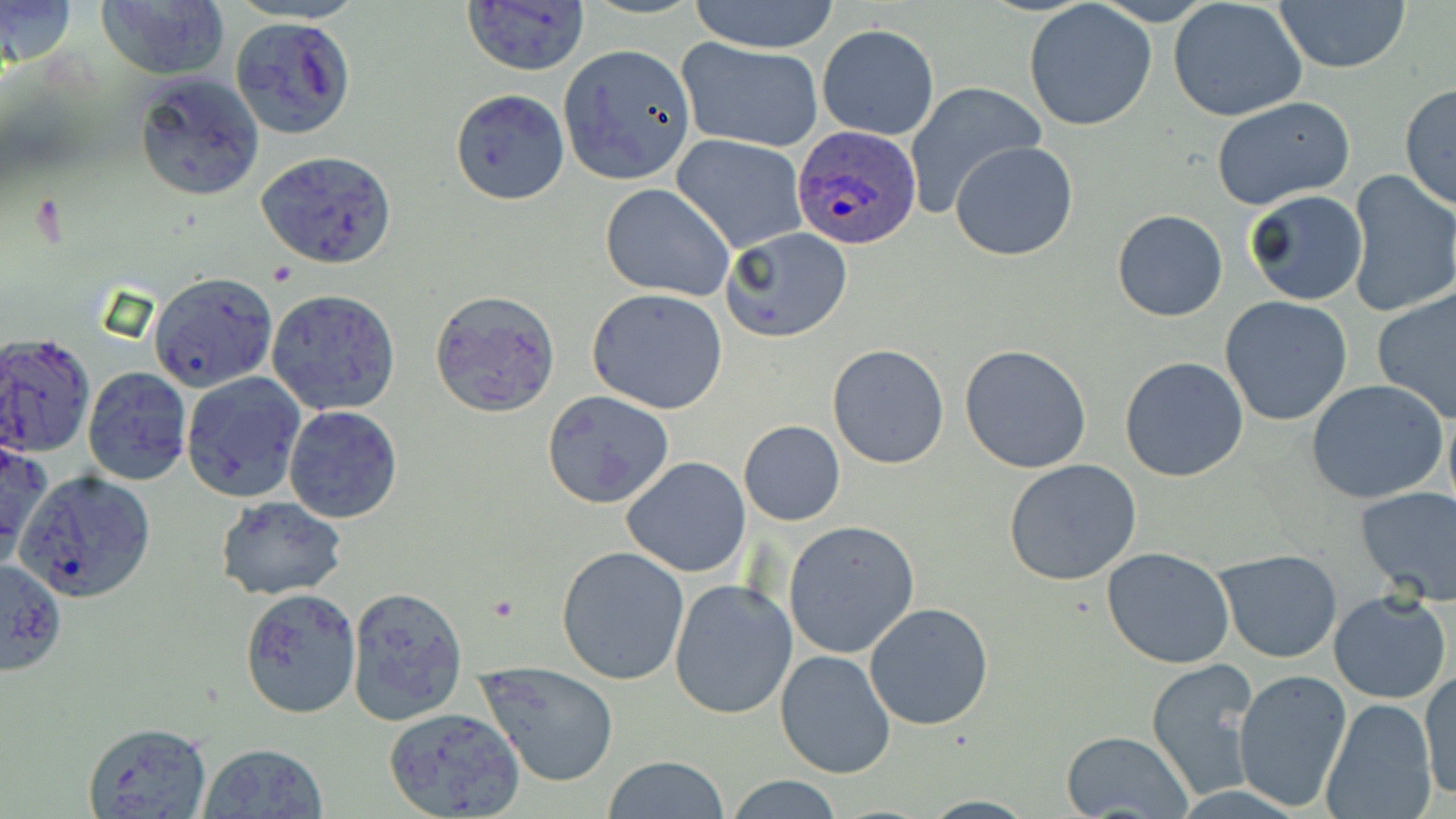 Approximate bounding boxes as (x1, y1, x2, y2) in pixels. Plasmodium ovale-infected red blood cell locations: (792, 123, 926, 251). Uninfected red blood cell locations: (0, 0, 78, 69), (464, 0, 588, 74), (688, 0, 838, 53), (1272, 0, 1412, 72), (1169, 1, 1307, 122), (96, 2, 229, 81), (1022, 2, 1158, 132), (230, 18, 357, 140), (818, 23, 940, 140), (678, 38, 825, 154), (559, 44, 697, 183), (137, 74, 263, 201), (903, 81, 1043, 218), (1399, 82, 1456, 211), (449, 88, 569, 206), (1210, 94, 1357, 209), (670, 133, 809, 254), (950, 141, 1078, 261), (256, 150, 397, 269), (1346, 170, 1456, 319), (600, 183, 733, 300), (1244, 189, 1368, 307), (1112, 208, 1228, 322), (723, 227, 853, 342), (147, 270, 278, 392), (1373, 287, 1456, 424), (266, 288, 403, 416), (588, 289, 729, 414), (430, 290, 561, 417), (1219, 295, 1353, 425), (0, 334, 95, 457), (959, 343, 1093, 473), (827, 345, 949, 468), (1120, 356, 1250, 483), (82, 366, 191, 486), (180, 371, 305, 502), (1305, 379, 1450, 505), (542, 390, 675, 510), (284, 404, 403, 524), (739, 420, 846, 526), (1, 434, 48, 568), (620, 456, 751, 576), (1003, 458, 1143, 585), (18, 470, 156, 603), (1353, 486, 1456, 605), (214, 496, 349, 600), (783, 520, 920, 658), (1101, 546, 1236, 669), (556, 547, 690, 686), (1215, 547, 1343, 664), (0, 557, 67, 675), (669, 580, 799, 720), (345, 584, 469, 725), (239, 587, 361, 718), (1328, 592, 1452, 705), (864, 602, 994, 730), (773, 648, 896, 779), (1145, 658, 1264, 801), (478, 661, 619, 787), (1234, 668, 1352, 810), (1418, 670, 1455, 802), (1321, 698, 1436, 819), (384, 706, 525, 818), (81, 722, 212, 818), (1060, 730, 1194, 816), (199, 741, 329, 819), (603, 756, 731, 818), (725, 774, 846, 818). Slide-level diagnosis: Plasmodium ovale. 1000x magnification. Image is 1456×819 pixels. May-Grünwald-Giemsa stain. Thin blood smear. Optical microscopy. One field of a larger specimen.